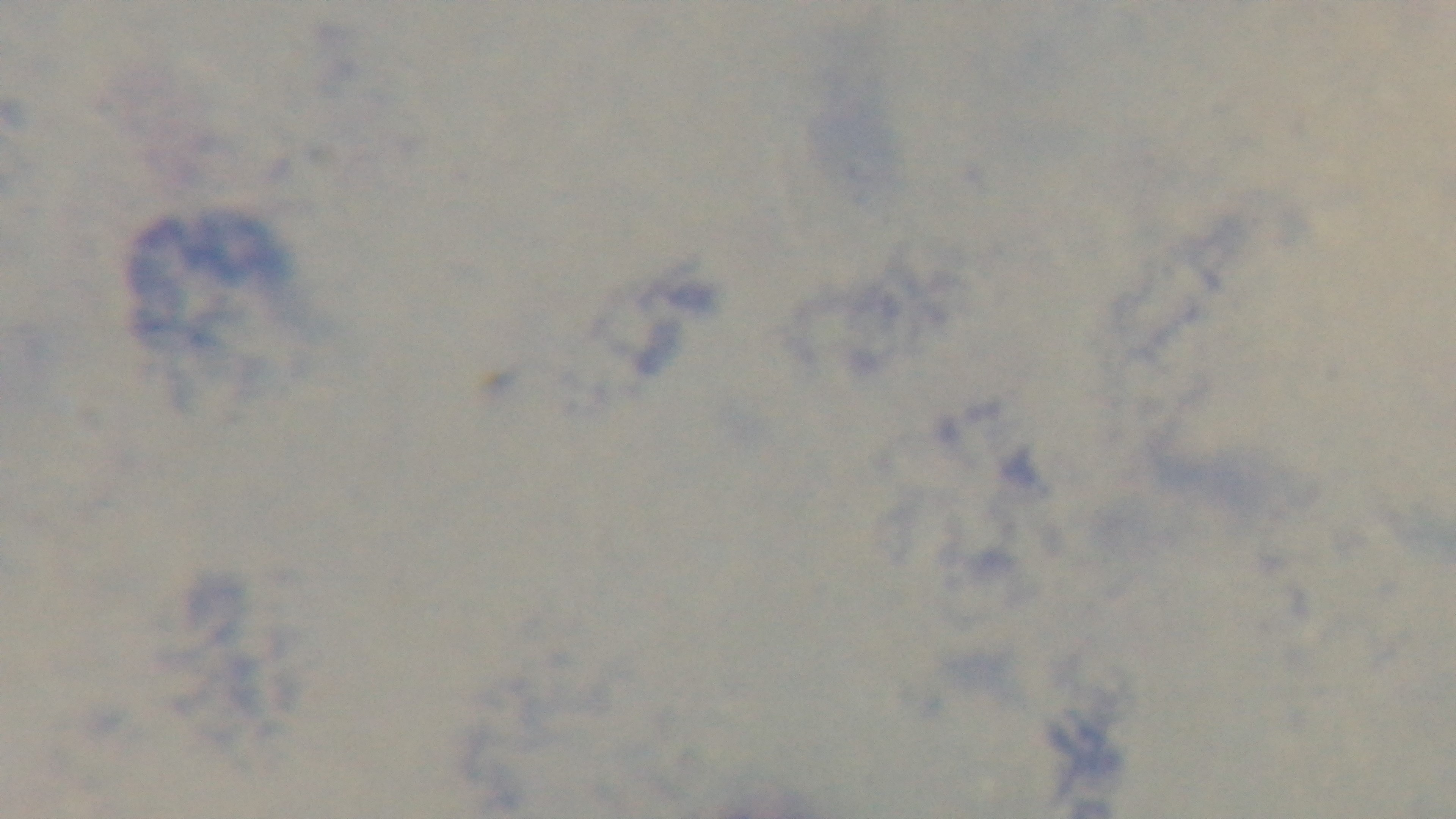
objective = 100x oil immersion
stain = Giemsa
malaria status = negative
modality = light microscopy
capture = mounted 4K digital camera
preparation = thick smear
field of view = one from the slide